Classify this cell by malaria status.
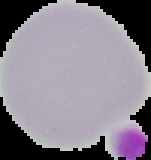
Uninfected.

The area outside the segmented cell region is set to black. Image is 151×160 pixels. From a thin blood smear.